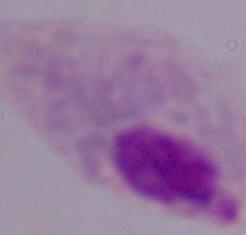

Summary:
  - Magnification: 1000x
  - Identification: trichomonad
  - Modality: micrograph